Comment on the morphology of the red blood cells.
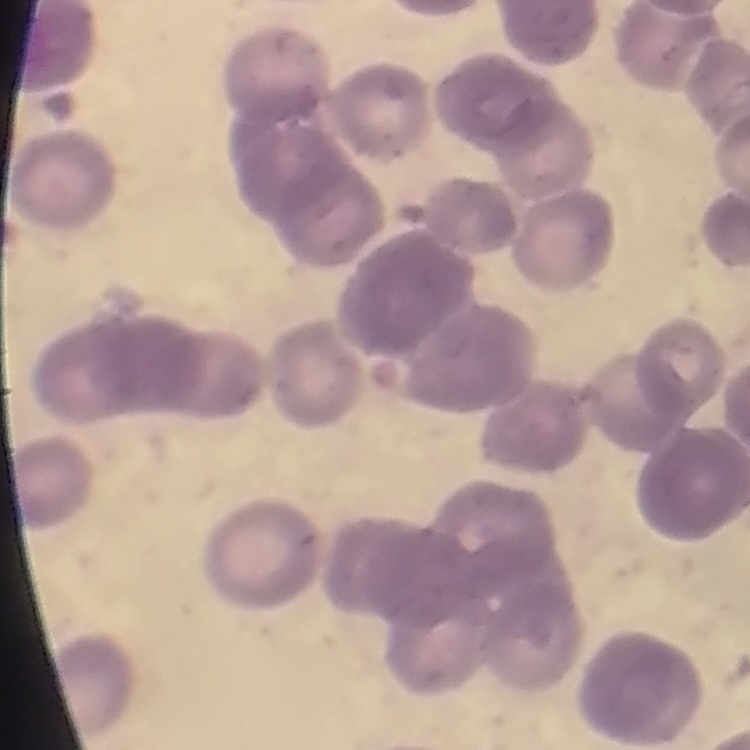

They show rouleaux formation.

Summary:
  - Image type: square crop of a larger photomicrograph
  - Preparation: thin peripheral smear
  - Stain: Field's or Giemsa